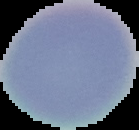

Cell region segmented out of the field of view; the surrounding area is masked to black. From a thin blood smear. Image is 139×130 pixels. Result: no Plasmodium parasites detected.